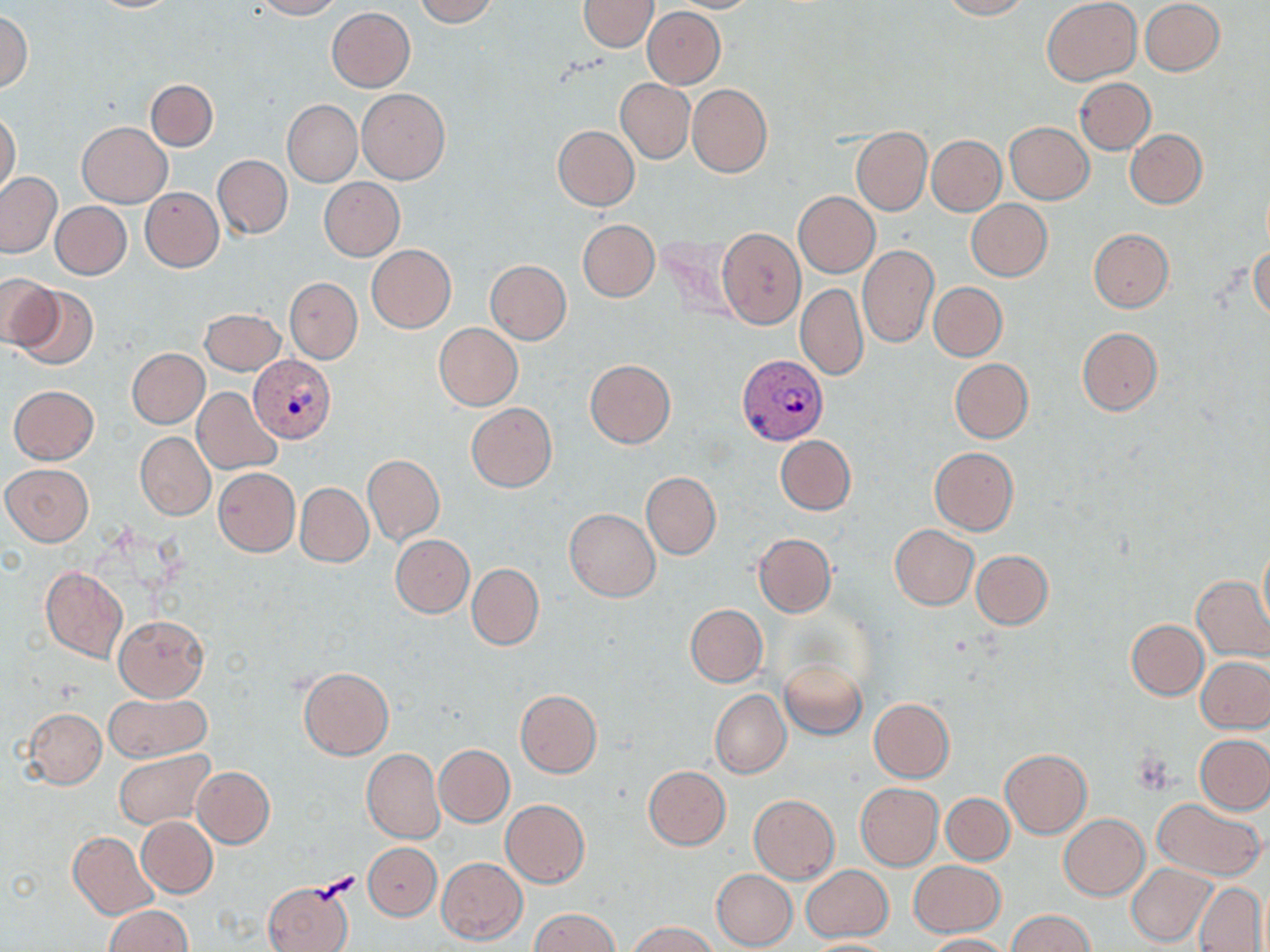
slide-level diagnosis = Plasmodium vivax
magnification = 1000x
image size = 1270×952 pixels
preparation = thin blood smear
Plasmodium vivax-infected red blood cell locations = approximate bounding boxes as (x1, y1, x2, y2) in pixels: (737, 354, 829, 445), (250, 356, 336, 441)
uninfected red blood cell locations = approximate bounding boxes as (x1, y1, x2, y2) in pixels: (252, 0, 341, 19), (412, 0, 499, 26), (578, 0, 658, 52), (667, 0, 762, 14), (941, 0, 1029, 19), (1041, 0, 1142, 85), (1139, 0, 1225, 76), (87, 1, 180, 12), (643, 6, 726, 88), (326, 7, 415, 91), (0, 10, 33, 94), (1074, 78, 1155, 154), (146, 79, 218, 150), (616, 79, 694, 163), (687, 83, 772, 178), (356, 88, 449, 183), (283, 100, 361, 186), (0, 111, 20, 197), (76, 121, 172, 207), (1005, 121, 1095, 204), (551, 125, 639, 210), (851, 127, 931, 215), (1124, 129, 1207, 208), (927, 134, 1005, 215), (212, 154, 292, 239), (0, 172, 63, 258), (319, 178, 403, 260), (139, 187, 223, 271), (793, 191, 879, 277), (966, 200, 1053, 280), (52, 201, 130, 279), (577, 219, 659, 301), (717, 228, 807, 329), (1088, 228, 1172, 312), (1250, 243, 1270, 322), (366, 244, 456, 333), (858, 245, 939, 348), (485, 259, 571, 344), (0, 273, 58, 350), (285, 277, 362, 364), (796, 282, 868, 380), (929, 282, 1007, 361), (11, 283, 99, 368), (199, 308, 286, 375), (434, 323, 522, 410), (1077, 327, 1163, 415), (127, 347, 209, 428), (949, 358, 1033, 443), (584, 359, 675, 448), (8, 384, 98, 464), (193, 388, 282, 474), (466, 403, 556, 493), (136, 433, 215, 519), (775, 435, 855, 515), (929, 446, 1018, 535), (362, 453, 445, 546), (2, 464, 93, 546), (213, 467, 300, 557), (641, 471, 720, 560), (296, 482, 372, 567), (564, 508, 660, 601), (889, 524, 979, 610), (754, 533, 836, 618), (390, 534, 474, 617), (1257, 539, 1269, 633), (971, 550, 1053, 629), (466, 562, 544, 651), (40, 566, 127, 663), (1192, 577, 1270, 661), (1129, 598, 1270, 691), (685, 604, 767, 687), (114, 615, 209, 701), (1126, 619, 1208, 699), (1197, 656, 1269, 733), (779, 657, 866, 738), (297, 666, 393, 759), (515, 689, 602, 778), (710, 691, 790, 778), (103, 693, 210, 761), (867, 698, 954, 783), (24, 708, 106, 788), (1196, 734, 1270, 813), (434, 744, 514, 827), (114, 748, 214, 830), (362, 749, 444, 845), (999, 749, 1092, 837), (192, 766, 274, 847), (644, 766, 730, 850), (854, 783, 943, 870), (941, 793, 1014, 865), (749, 794, 839, 883), (927, 794, 1009, 935), (501, 799, 589, 888), (1153, 799, 1264, 881), (1059, 814, 1150, 899), (137, 817, 218, 897), (68, 831, 158, 918), (363, 843, 440, 920), (436, 858, 527, 944), (910, 861, 1005, 937), (1128, 864, 1216, 945), (802, 866, 892, 940), (711, 868, 798, 950), (262, 880, 354, 952), (1193, 882, 1267, 952), (106, 906, 192, 952), (531, 908, 617, 952), (1008, 910, 1093, 952), (628, 921, 716, 952), (922, 934, 1010, 952), (801, 938, 900, 951)
modality = light microscopy
stain = May-Grünwald-Giemsa
field of view = one of a larger specimen